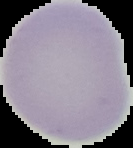

preparation = thin blood smear
malaria status = uninfected
image size = 133×148 pixels
image type = segmented cell region on a black background